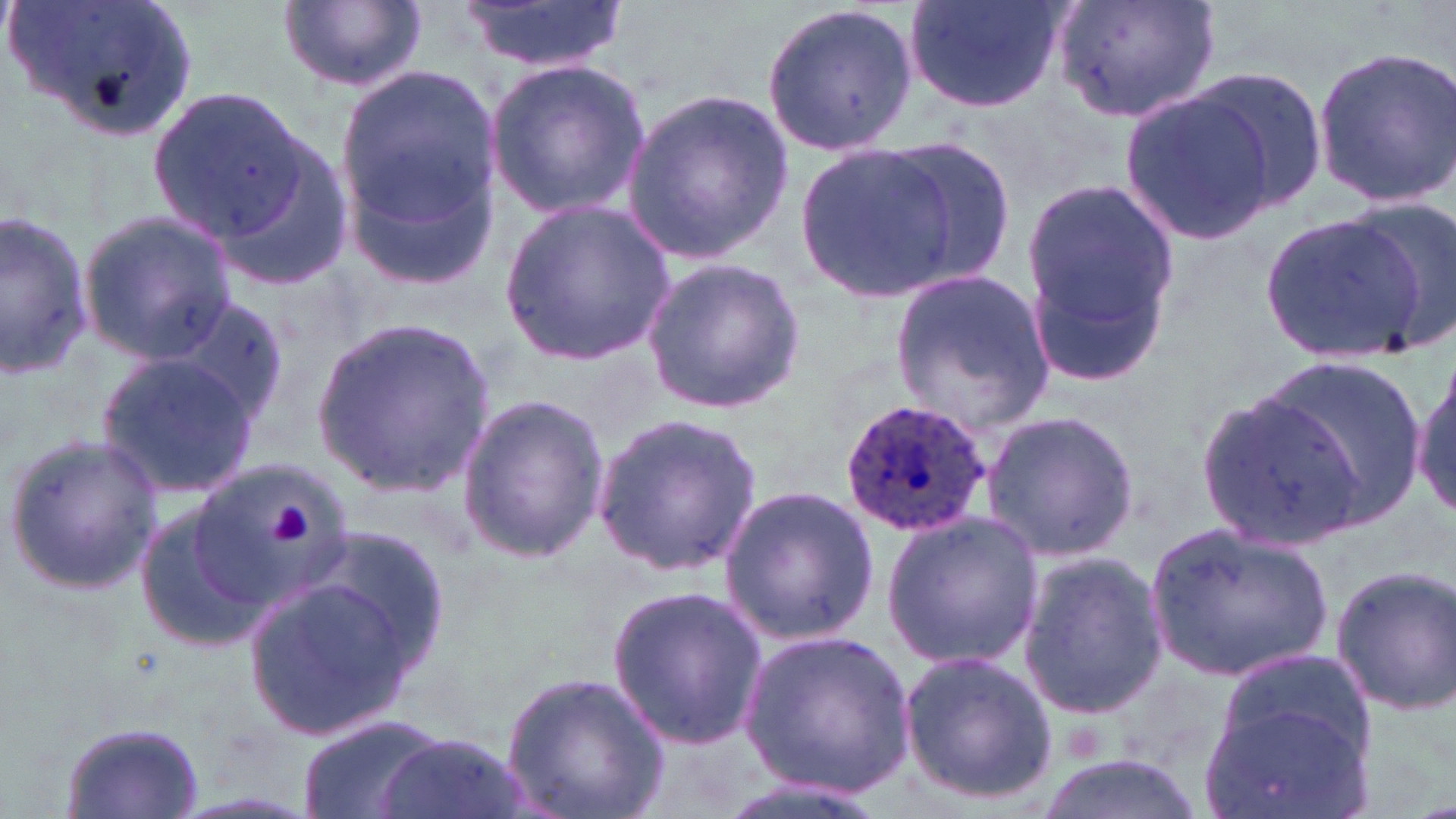

Summary:
  - Coordinate format: approximate bounding boxes as (x1,y1)-(x2,y2) corner pairs in pixels
  - Plasmodium ovale-infected red blood cell locations: (840,398)-(992,540)
  - Uninfected red blood cell locations: (9,0)-(193,141), (460,0)-(626,75), (902,0)-(1067,113), (1049,0)-(1226,125), (280,1)-(426,95), (761,1)-(918,158), (1311,44)-(1456,207), (485,58)-(652,219), (335,62)-(503,257), (1184,63)-(1329,217), (1117,82)-(1279,246), (148,86)-(314,246), (622,86)-(797,268), (886,136)-(1020,293), (791,139)-(964,303), (1019,175)-(1177,379), (501,199)-(674,365), (1348,199)-(1456,355), (1260,208)-(1435,365), (78,211)-(238,365), (0,212)-(97,379), (640,256)-(805,413), (889,266)-(1055,439), (176,297)-(296,433), (308,315)-(497,496), (96,350)-(260,501), (1251,355)-(1429,524), (1411,358)-(1455,522), (1198,390)-(1366,547), (454,393)-(610,563), (981,407)-(1142,563), (589,408)-(762,581), (3,433)-(164,596), (190,451)-(350,608), (717,481)-(882,648), (134,500)-(272,653), (881,510)-(1043,670), (1147,520)-(1333,685), (307,527)-(448,675), (1016,549)-(1169,720), (1327,563)-(1456,718), (243,573)-(423,745), (604,581)-(771,753), (737,628)-(914,801), (895,648)-(1060,807), (1216,649)-(1375,777), (499,668)-(670,819), (1203,701)-(1369,819), (296,712)-(450,819), (61,721)-(207,819), (377,732)-(525,819), (1029,753)-(1211,819)
  - Platelet locations: (271,504)-(313,545)
  - Slide-level diagnosis: Plasmodium ovale
  - Magnification: 1000x
  - Modality: optical microscopy
  - Preparation: thin blood smear
  - Field of view: one of a larger specimen
  - Stain: May-Grünwald-Giemsa
  - Image size: 1456×819 pixels